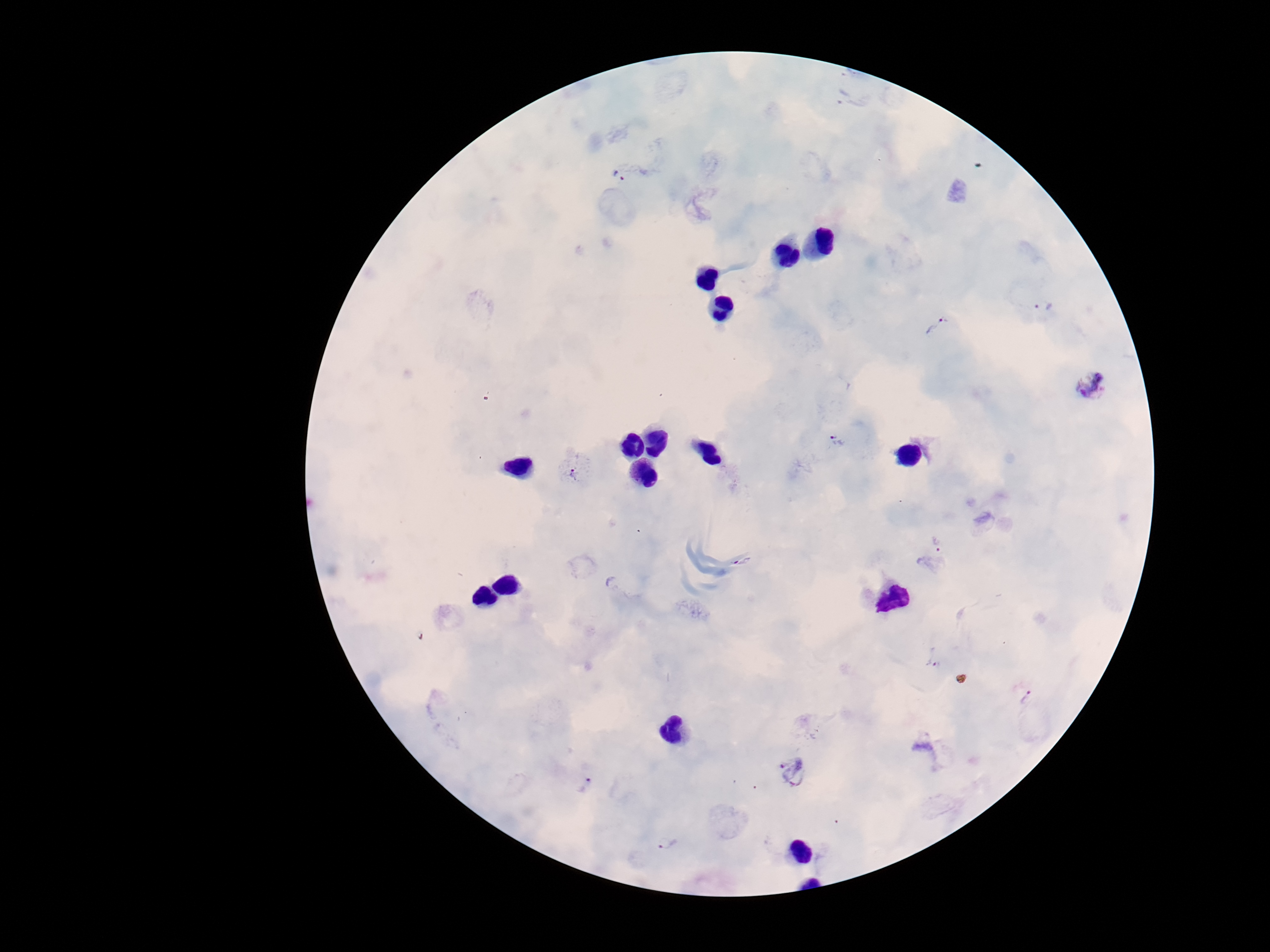

Approximate object centers, in pixels from the top-left corner.
Summary:
  - Plasmodium parasite locations: (x=619, y=175), (x=1044, y=308), (x=939, y=328), (x=1094, y=383), (x=837, y=441), (x=575, y=474), (x=938, y=544), (x=743, y=561), (x=934, y=662), (x=1028, y=697), (x=793, y=770), (x=586, y=784), (x=669, y=842)
  - Image size: 1270×952 pixels
  - Patient malaria status: positive
  - Field of view: single
  - Stain: Giemsa
  - Preparation: thick peripheral-blood smear
  - Capture: smartphone camera through the microscope eyepiece
  - Magnification: 100x